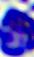

{
  "identification": "leukocyte",
  "modality": "micrograph",
  "magnification": "400x"
}